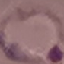 Result: malaria parasites detected. Photographed with a smartphone camera at the microscope eyepiece. Thin blood smear. Giemsa-stained preparation. Automatically extracted cell patch, resized to 64 × 64 pixels.